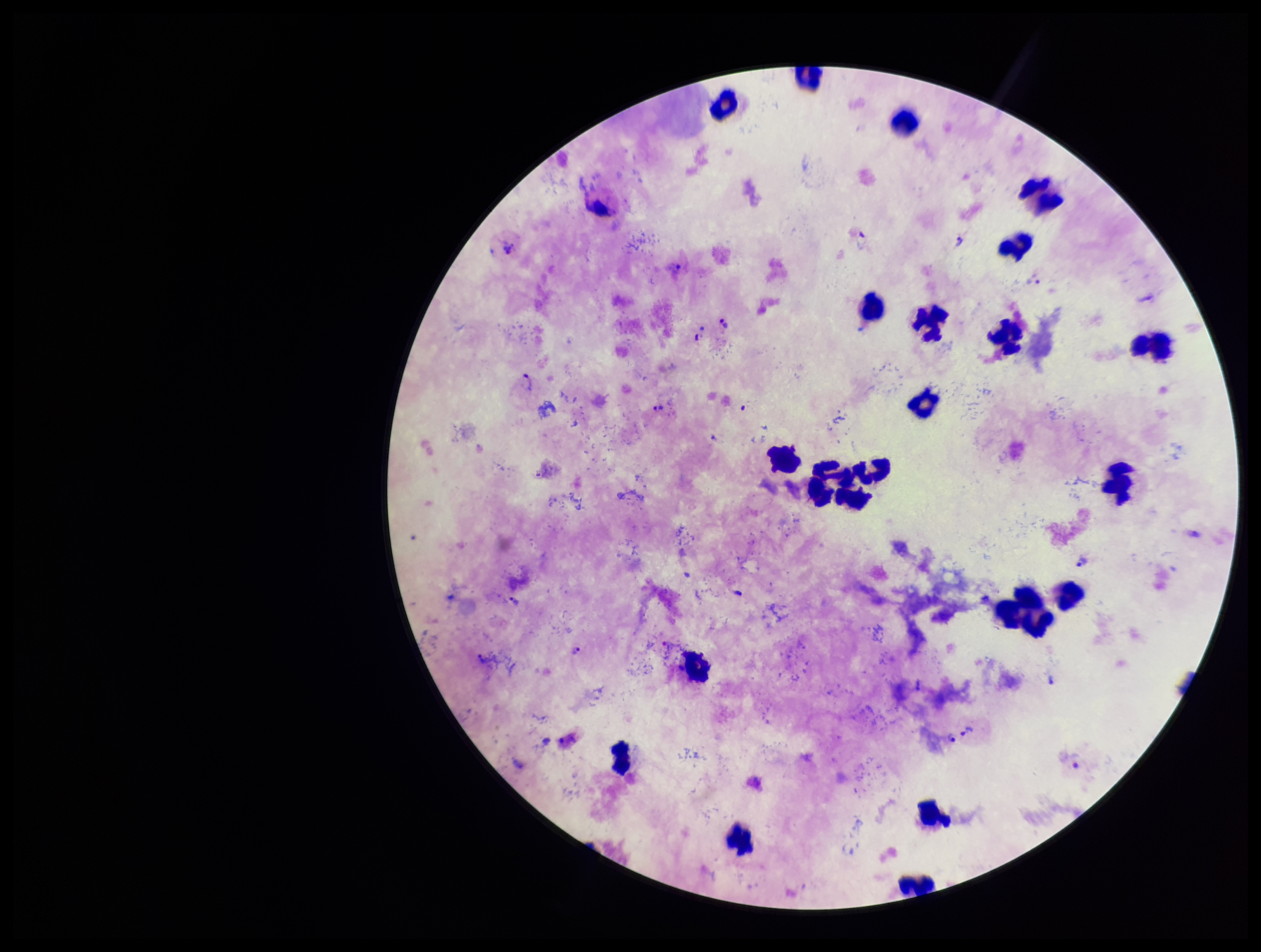
{
  "species_reported_for_this_patient": "Plasmodium vivax",
  "parasite_count": 12,
  "preparation": "thick",
  "plasmodium_parasites": "identified",
  "stain": "Giemsa",
  "image_size": "1261×952 pixels",
  "patient_malaria_status": "infected",
  "field_of_view": "one from this slide",
  "leukocyte_count": 22,
  "capture": "smartphone photograph through the microscope eyepiece"
}